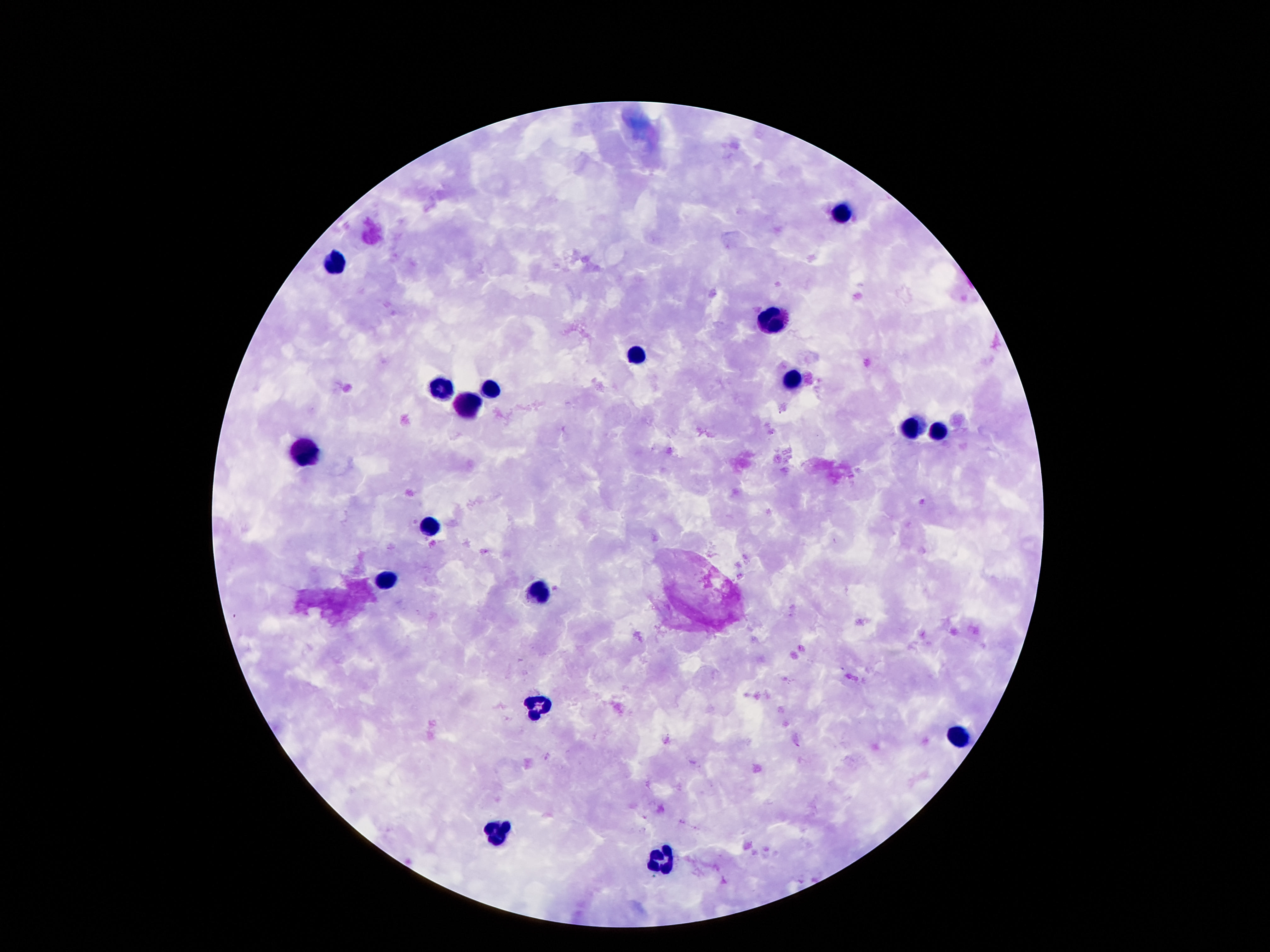
{
  "leukocyte_locations": "approximate centers as [x, y] in pixels: [841, 214], [335, 265], [772, 319], [635, 355], [794, 380], [491, 389], [438, 391], [465, 403], [907, 429], [938, 432], [308, 453], [432, 529], [390, 582], [536, 595], [540, 703], [956, 737], [496, 830], [664, 863]",
  "stain": "Giemsa",
  "image_size": "1270×952 pixels",
  "preparation": "thick peripheral-blood smear",
  "capture": "smartphone camera through the microscope eyepiece",
  "field_of_view": "one from this slide",
  "magnification": "100x",
  "patient_malaria_status": "negative"
}